Locate every Trypanosoma brucei.
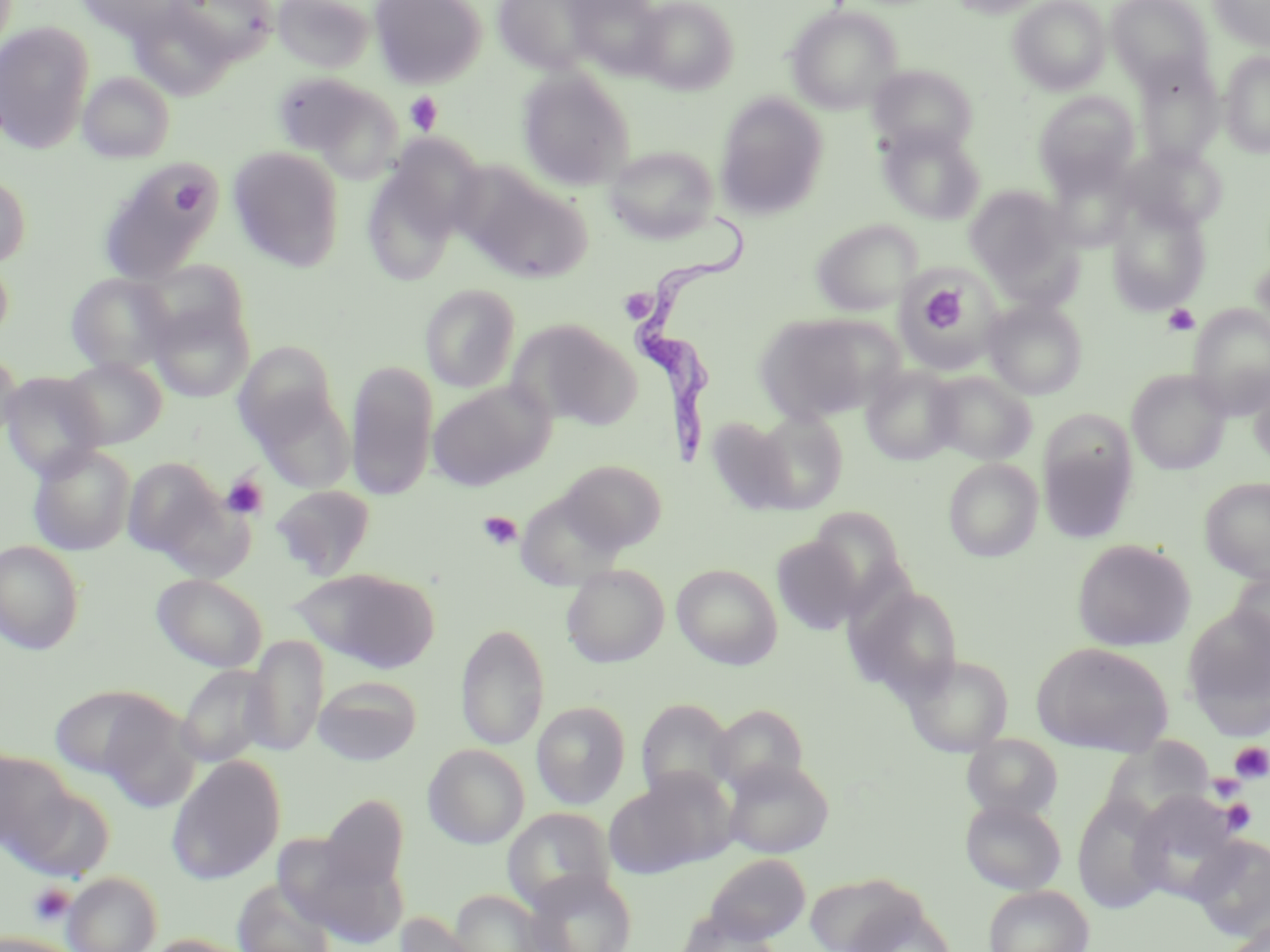
Approximate bounding boxes as (x1, y1, x2, y2) in pixels.
Trypanosoma brucei: (630, 215, 756, 461).

Summary:
  - Platelet locations: (406, 92, 443, 135), (171, 182, 205, 215), (917, 282, 972, 340), (618, 290, 661, 322), (1163, 304, 1200, 336), (221, 473, 269, 520), (477, 511, 522, 551), (1231, 742, 1270, 783), (1208, 772, 1245, 801), (1221, 799, 1256, 835), (28, 883, 75, 926)
  - Uninfected red blood cell locations: (73, 0, 187, 40), (169, 0, 277, 65), (273, 0, 374, 73), (370, 0, 486, 88), (493, 0, 601, 74), (565, 0, 667, 77), (634, 0, 738, 93), (946, 0, 1049, 18), (1009, 0, 1110, 94), (1106, 0, 1214, 88), (1209, 0, 1270, 50), (129, 3, 235, 100), (786, 5, 902, 114), (0, 22, 94, 154), (1220, 51, 1270, 157), (1134, 57, 1224, 166), (867, 64, 977, 155), (517, 69, 635, 189), (79, 72, 176, 163), (273, 72, 402, 179), (1034, 92, 1141, 196), (716, 93, 828, 218), (877, 123, 986, 225), (375, 131, 487, 253), (603, 145, 720, 244), (1122, 145, 1227, 233), (228, 146, 344, 272), (99, 159, 222, 280), (1045, 161, 1136, 251), (361, 163, 464, 287), (464, 168, 594, 283), (0, 171, 31, 269), (964, 186, 1072, 286), (1106, 198, 1211, 314), (811, 219, 922, 315), (0, 250, 14, 347), (1249, 254, 1270, 345), (139, 259, 250, 355), (65, 272, 177, 375), (900, 273, 998, 367), (420, 283, 521, 392), (149, 298, 254, 402), (982, 298, 1088, 399), (1188, 305, 1270, 418), (755, 313, 893, 424), (509, 320, 639, 430), (232, 340, 339, 447), (0, 351, 21, 445), (61, 358, 167, 449), (345, 361, 438, 501), (861, 365, 962, 465), (1248, 368, 1270, 470), (926, 370, 1037, 465), (1127, 370, 1231, 474), (1, 371, 106, 480), (428, 380, 554, 491), (251, 388, 355, 495), (753, 410, 848, 512), (705, 416, 797, 516), (1039, 435, 1136, 544), (26, 443, 136, 556), (122, 456, 226, 560), (943, 458, 1043, 562), (558, 459, 667, 553), (1200, 477, 1270, 583), (271, 484, 376, 580), (808, 506, 909, 615), (772, 536, 863, 635), (1071, 538, 1196, 652), (0, 540, 85, 654), (672, 563, 783, 669), (561, 564, 670, 668), (1228, 566, 1270, 666), (293, 568, 439, 672), (151, 573, 267, 672), (849, 583, 965, 703), (1181, 604, 1270, 738), (455, 623, 549, 750), (243, 635, 329, 756), (1031, 642, 1175, 757), (902, 652, 1014, 756), (175, 665, 274, 769), (313, 676, 421, 766), (48, 684, 175, 781), (635, 697, 737, 804), (93, 700, 202, 811), (532, 702, 630, 810), (708, 704, 809, 798), (962, 733, 1063, 822), (422, 744, 530, 849), (0, 752, 76, 856), (167, 756, 286, 885), (723, 757, 834, 859), (604, 775, 723, 877), (11, 782, 117, 882), (1129, 792, 1243, 905), (1072, 793, 1169, 914), (321, 795, 409, 893), (959, 798, 1067, 895), (502, 807, 617, 911), (1187, 834, 1270, 944), (295, 846, 408, 947), (703, 853, 811, 945), (523, 869, 638, 952), (803, 870, 930, 950), (62, 871, 162, 952), (232, 880, 337, 952), (983, 885, 1093, 952), (448, 889, 556, 952), (845, 903, 959, 952), (396, 912, 485, 952), (676, 912, 786, 952), (0, 931, 82, 952), (143, 935, 255, 952)
  - Slide-level diagnosis: Trypanosoma brucei
  - Stain: May-Grünwald-Giemsa
  - Preparation: thin blood smear
  - Field of view: one of a larger specimen
  - Magnification: 1000x
  - Modality: optical microscopy
  - Image size: 1270×952 pixels